Point out malaria parasites and leukocytes.
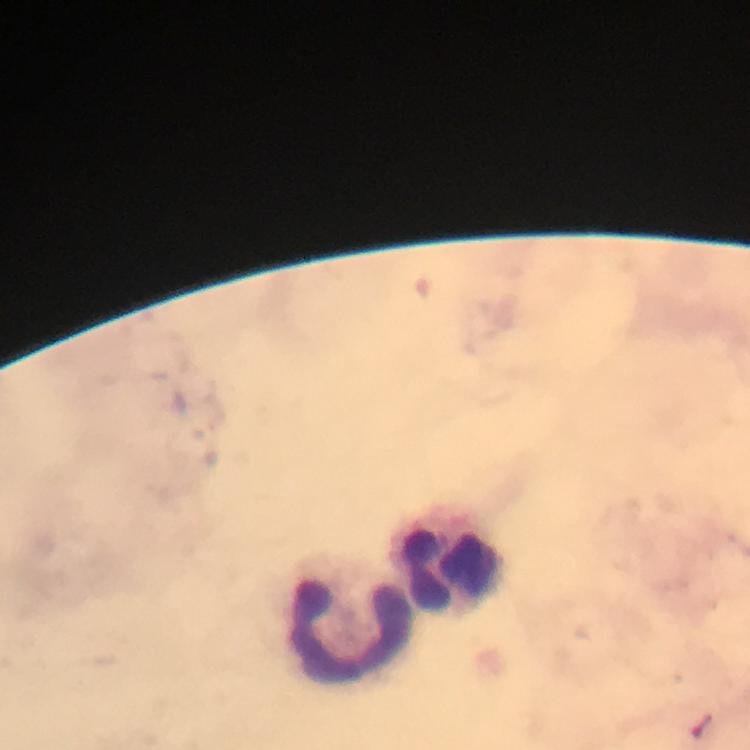
No malaria parasites seen.
Approximate centers as {x, y} in pixels.
Leukocytes: {451, 570}, {347, 629}.

Immersion oil was used. From a malaria diagnostic workup. 100x magnification. Thick blood film. Giemsa-stained preparation. Smartphone photograph taken through a microscope. Image is 750×750 pixels. A crop from one field of view.